Locate every blood parasite and identify its species.
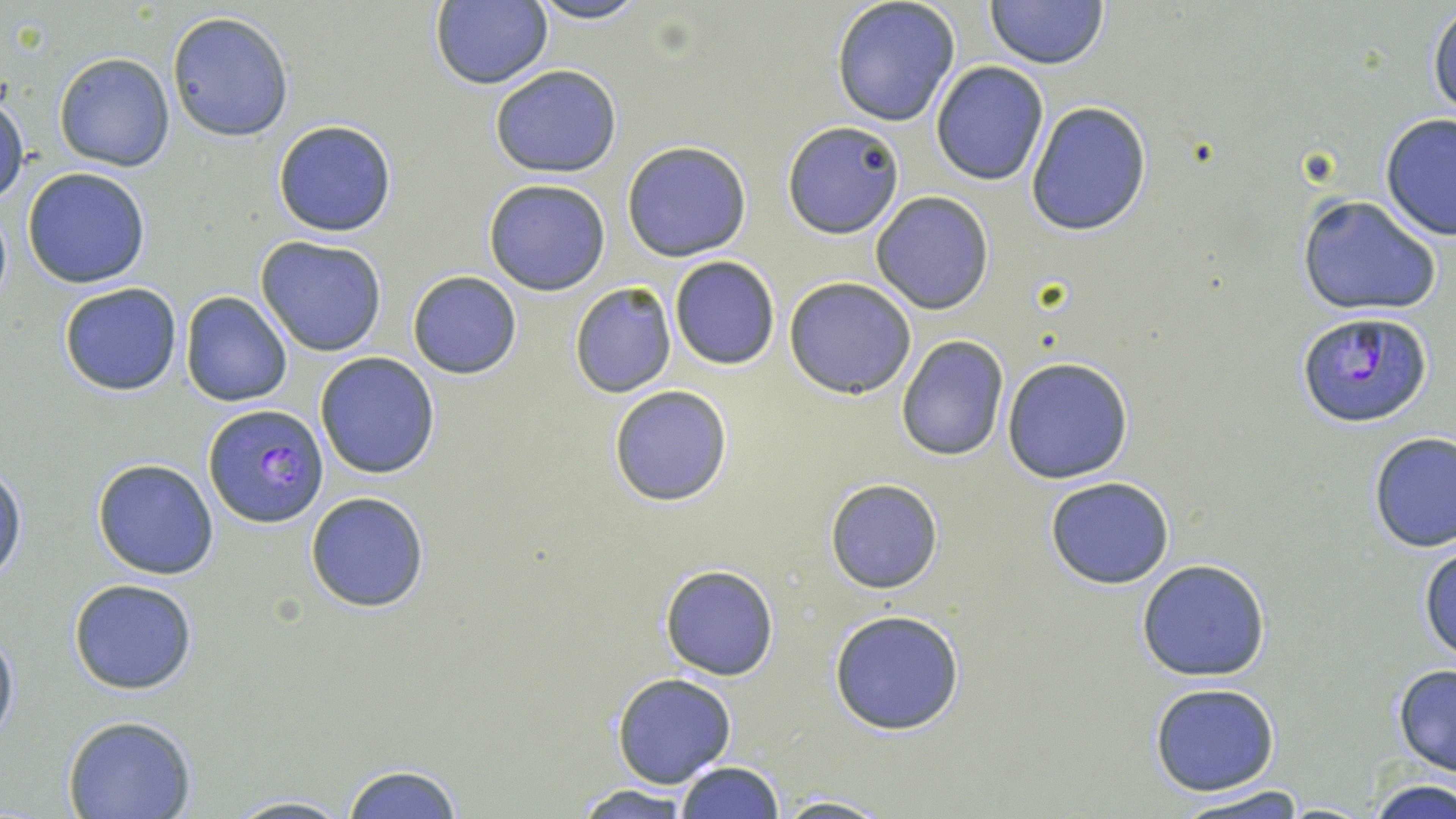
Approximate bounding boxes as (x1, y1, x2, y2) in pixels.
Plasmodium falciparum-infected red blood cells: (1295, 311, 1435, 428), (203, 404, 329, 527).
No Plasmodium ovale, Plasmodium malariae, Plasmodium vivax, Babesia divergens, or Trypanosoma brucei observed.

slide-level diagnosis = Plasmodium falciparum
modality = light microscopy
image size = 1456×819 pixels
stain = May-Grünwald-Giemsa
field of view = single
preparation = thin blood smear
magnification = 1000x
uninfected red blood cell locations = approximate bounding boxes as (x1, y1, x2, y2) in pixels: (525, 0, 652, 25), (830, 0, 961, 127), (985, 0, 1109, 70), (429, 1, 553, 89), (1427, 4, 1456, 121), (167, 11, 294, 141), (54, 52, 175, 172), (931, 61, 1048, 186), (489, 63, 622, 177), (0, 87, 28, 206), (1024, 99, 1151, 236), (1379, 114, 1456, 241), (272, 120, 397, 237), (782, 120, 904, 240), (622, 140, 753, 262), (21, 167, 150, 288), (483, 179, 612, 296), (870, 191, 995, 313), (1295, 194, 1443, 318), (256, 237, 386, 356), (668, 255, 780, 371), (407, 271, 522, 379), (784, 276, 917, 399), (58, 281, 183, 397), (568, 281, 678, 398), (180, 292, 294, 407), (896, 336, 1008, 461), (314, 352, 440, 478), (1002, 357, 1133, 483), (608, 385, 733, 506), (1366, 431, 1455, 553), (92, 458, 221, 579), (0, 465, 24, 585), (1045, 476, 1175, 589), (825, 479, 944, 594), (304, 490, 431, 612), (1418, 540, 1456, 664), (1136, 559, 1270, 681), (661, 565, 779, 681), (68, 578, 198, 695), (828, 608, 968, 735), (0, 620, 19, 751), (1390, 664, 1456, 779), (611, 674, 737, 788), (1149, 682, 1279, 795), (63, 716, 198, 819), (675, 762, 783, 818), (342, 764, 464, 818), (1366, 778, 1454, 819), (573, 785, 695, 819), (1171, 785, 1310, 819), (223, 793, 354, 819), (771, 793, 891, 818)